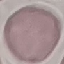

malaria status = uninfected
capture = smartphone through the microscope eyepiece
preparation = thin blood film
stain = Giemsa
image type = cell patch, automatically extracted from a larger field of view and resized to 64 × 64 pixels